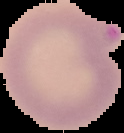
image_type: segmented cell region with the area outside set to black
preparation: thin blood film
image_size: 124×133 pixels
result: Plasmodium parasites identified